Locate every Plasmodium parasite.
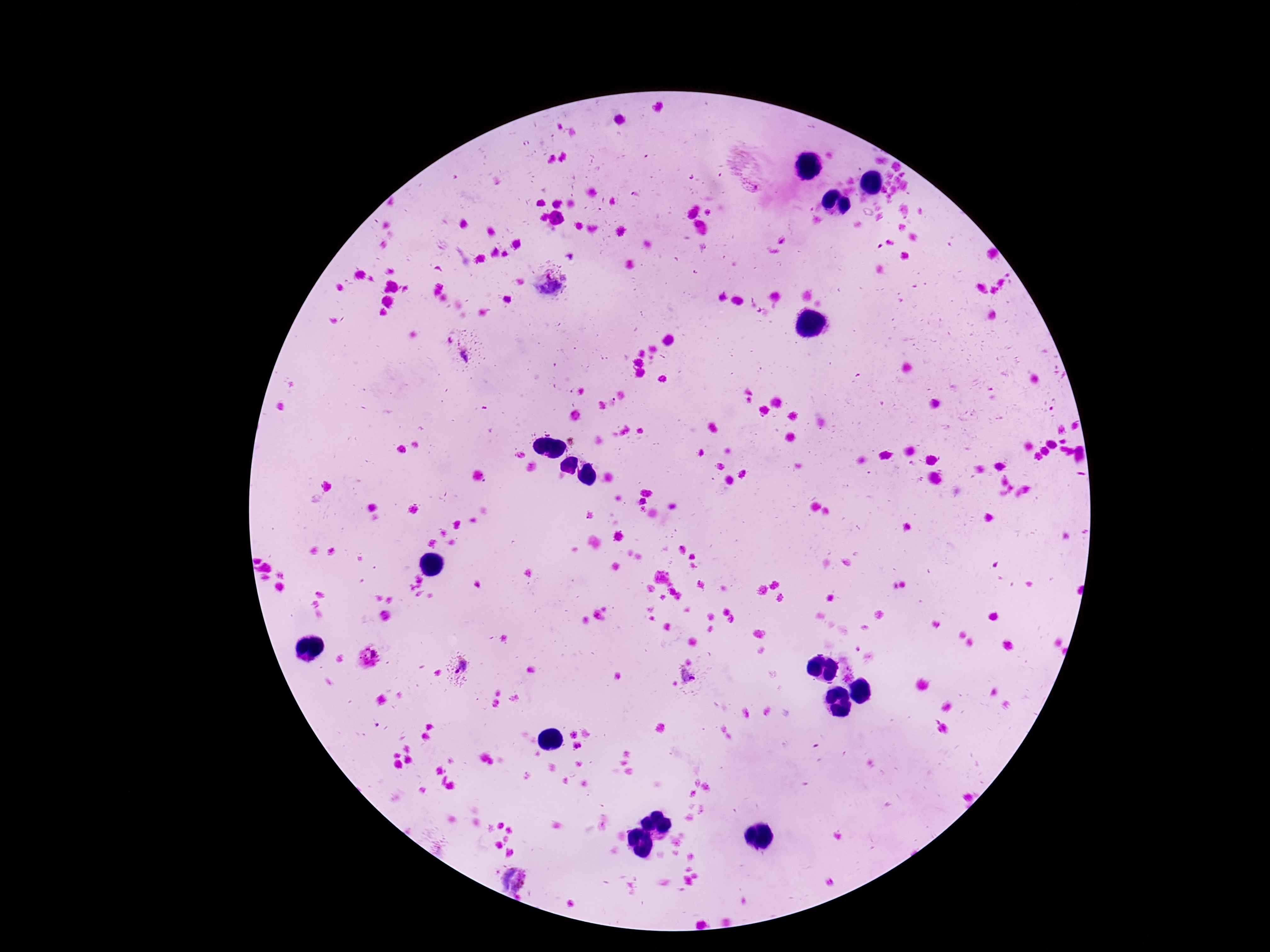

Approximate centers as (x, y) in pixels.
Plasmodium parasites: (552, 285), (467, 354), (368, 659), (462, 666), (847, 671), (690, 679), (513, 877).

stain = Giemsa
capture = smartphone camera through the microscope eyepiece
field of view = single
magnification = 100x
preparation = thick peripheral-blood smear
patient malaria status = infected
image size = 1270×952 pixels